Point out every malaria parasite and every leukocyte.
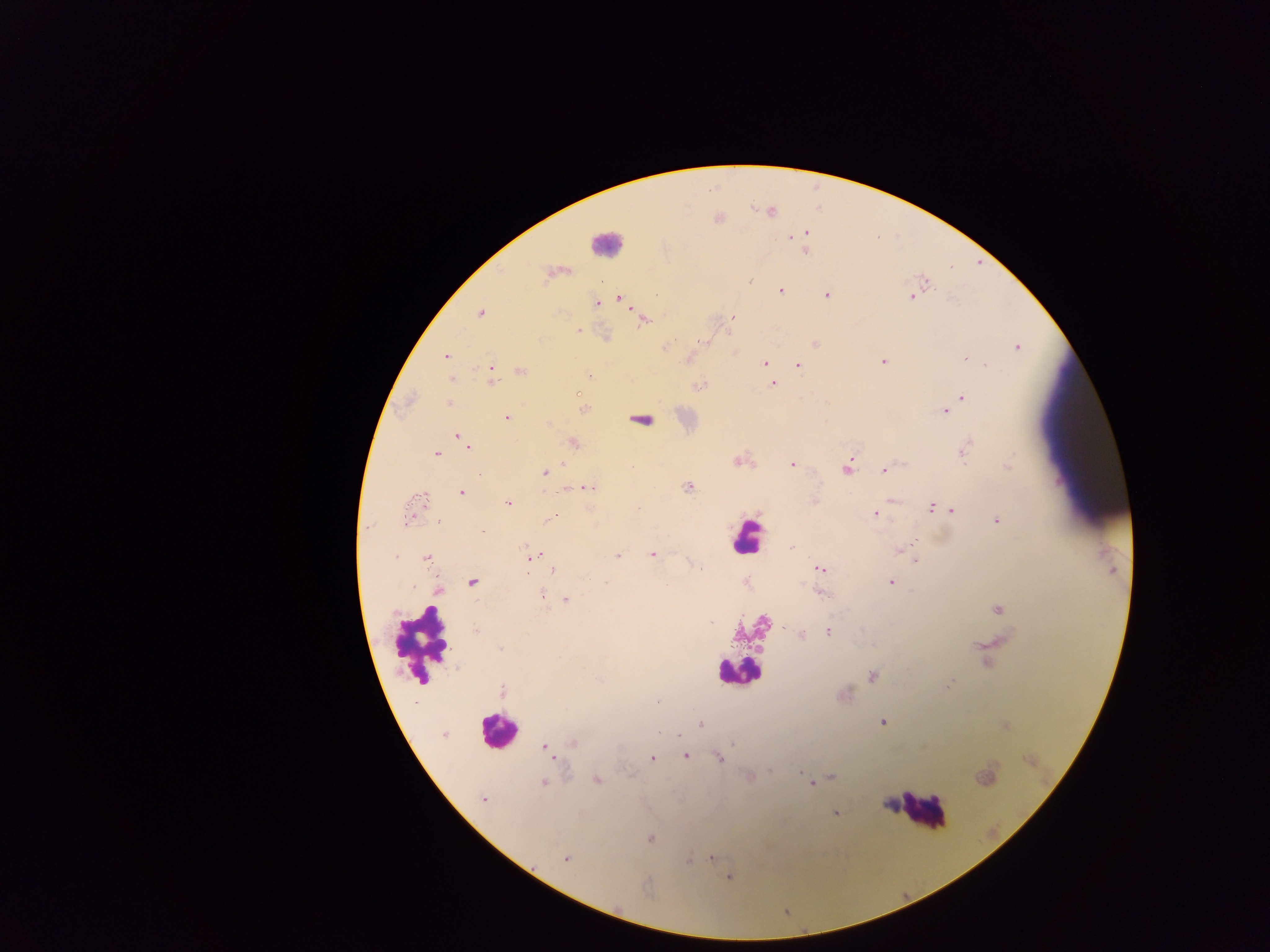

Approximate centers as (x, y) in pixels.
Malaria parasites: (806, 232), (791, 236), (805, 251), (749, 280), (926, 283), (780, 291), (827, 295), (912, 296), (619, 297), (596, 303), (480, 313), (732, 317), (644, 319), (578, 330), (704, 341), (816, 343), (666, 345), (1017, 347), (446, 357), (965, 358), (883, 361), (763, 363), (986, 365), (798, 366), (522, 372), (491, 373), (589, 375), (491, 380), (772, 383), (698, 386), (962, 398), (448, 403), (583, 409), (946, 412), (506, 417), (639, 420), (459, 437), (574, 443), (466, 444), (964, 451), (436, 453), (737, 461), (562, 464), (791, 464), (1008, 467), (846, 469), (883, 470), (545, 473), (688, 487), (588, 488), (462, 492), (421, 497), (814, 501), (508, 503), (932, 508), (638, 509), (952, 510), (875, 514), (552, 516), (407, 520), (439, 521), (996, 521), (913, 544), (792, 547), (901, 549), (652, 554), (397, 556), (532, 556), (617, 556), (426, 558), (915, 560), (700, 568), (553, 569), (820, 569), (472, 582), (605, 582), (891, 582), (439, 591), (822, 592), (541, 595), (566, 600), (998, 610), (477, 631), (828, 632), (801, 635), (501, 649), (871, 676), (949, 684), (503, 691), (700, 723), (883, 723), (659, 731), (443, 735), (679, 735), (572, 743), (733, 743), (545, 747), (686, 755), (652, 758), (719, 758), (770, 770), (800, 773), (831, 776), (597, 779), (544, 782), (811, 783), (483, 799), (836, 814), (650, 839), (567, 858), (711, 858), (688, 861), (729, 877).
Leukocytes: (605, 243), (747, 537), (422, 643), (736, 671), (497, 730), (920, 809).

Image is 1270×952 pixels. Mobile-phone photograph taken through the microscope. One field of view. Thick blood smear. Sample from Ghana.